Assess for malaria.
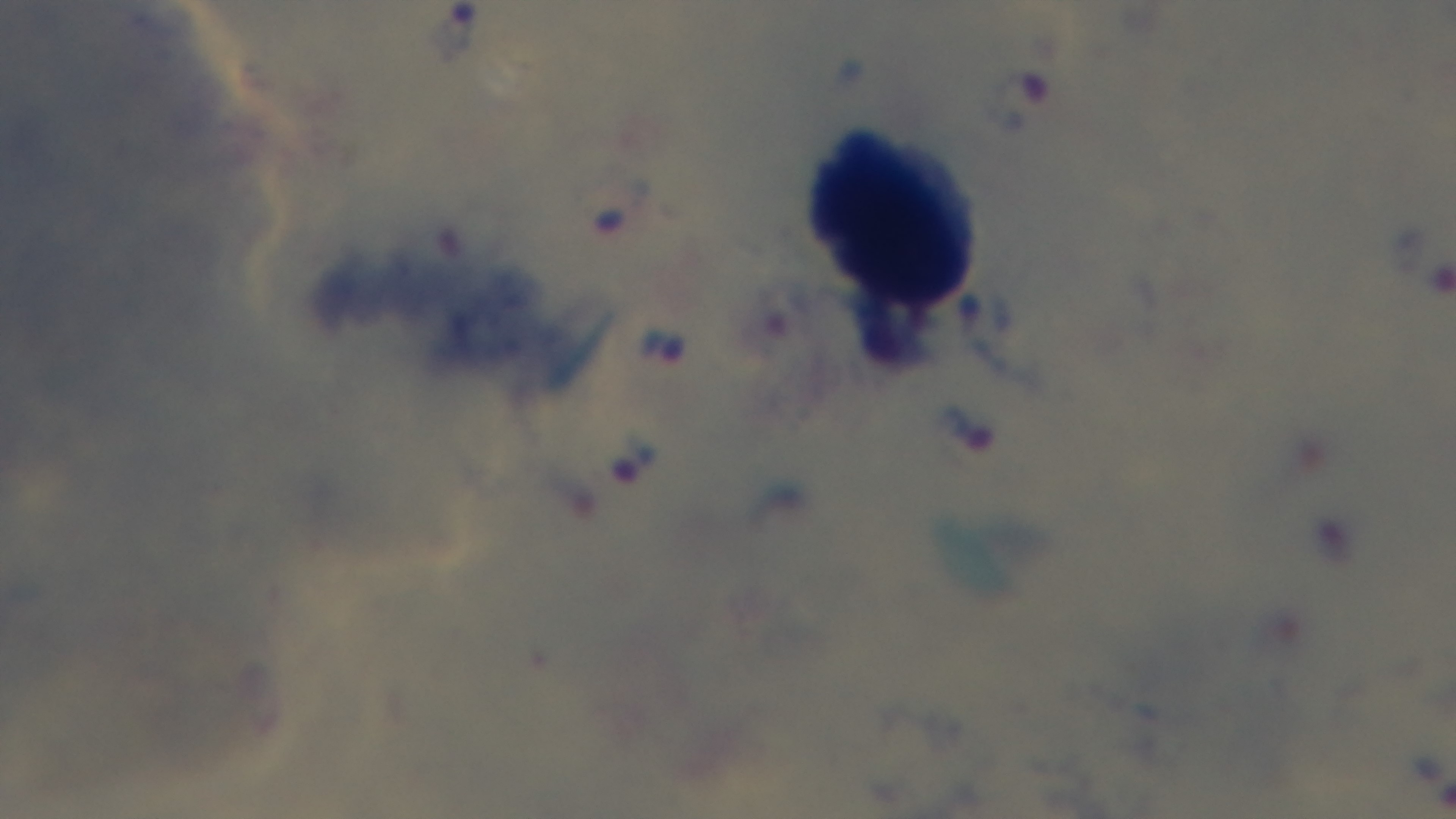
Infected.

Summary:
  - Modality: light microscopy
  - Preparation: thick smear
  - Objective: 100x oil immersion
  - Capture: mounted 4K digital camera
  - Stain: Giemsa
  - Field of view: single